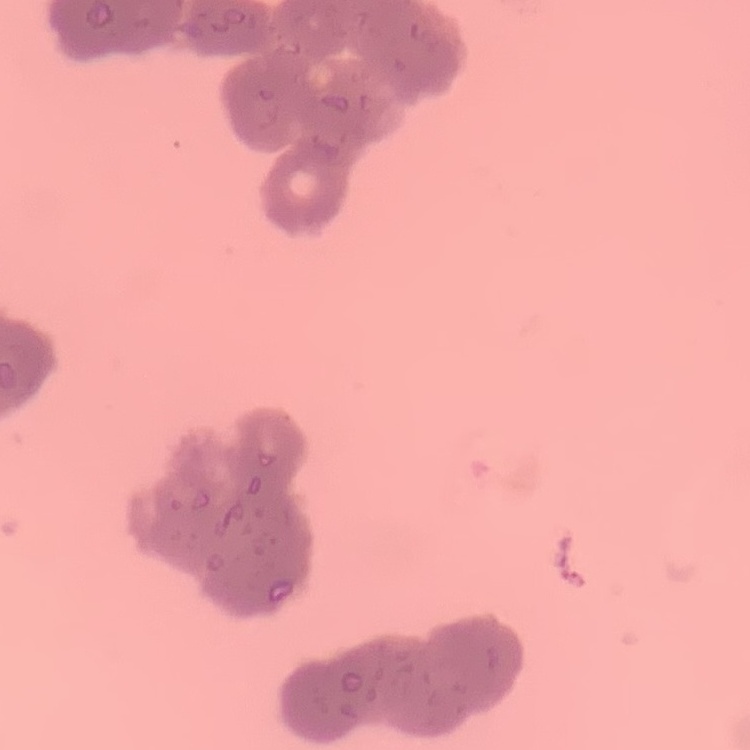
Summary:
  - Erythrocyte morphology: rouleaux formation
  - Stain: Field's or Giemsa
  - Preparation: thin blood smear
  - Image type: one tile cut from a larger photomicrograph